Identify the parasite.
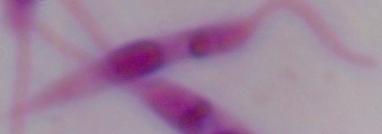
This is Leishmania.

{
  "magnification": "1000x",
  "modality": "photomicrograph"
}